Locate every Plasmodium ovale-infected red blood cell.
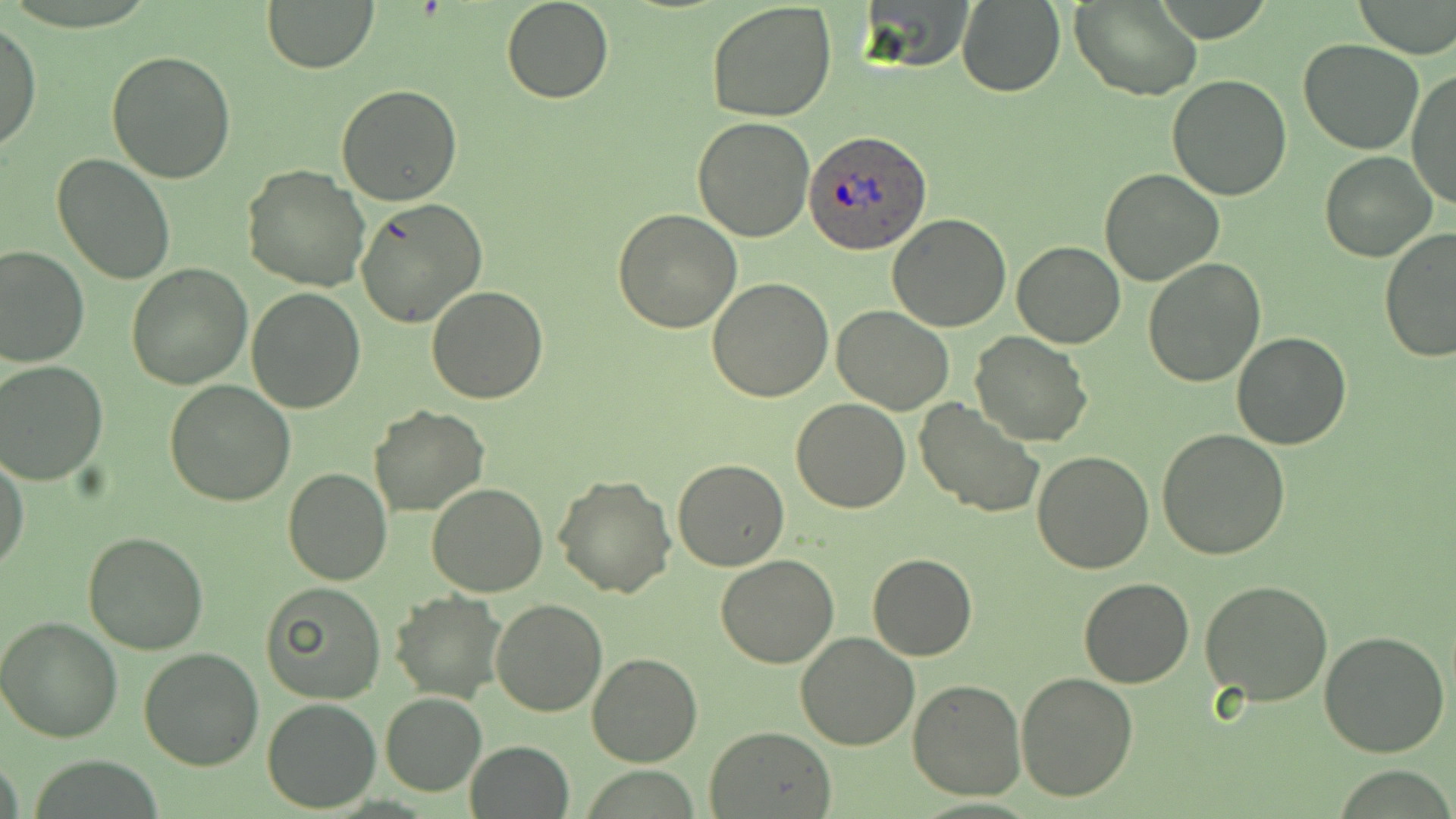

Approximate bounding boxes as [x1, y1, x2, y2] in pixels.
Plasmodium ovale-infected red blood cells: [804, 129, 932, 254].

{
  "slide_level_diagnosis": "Plasmodium ovale",
  "uninfected_red_blood_cell_locations": "approximate bounding boxes as [x1, y1, x2, y2] in pixels: [501, 0, 614, 104], [706, 0, 838, 120], [861, 0, 978, 72], [1352, 0, 1456, 58], [263, 1, 377, 73], [956, 1, 1067, 97], [1073, 2, 1202, 100], [1, 18, 40, 156], [1297, 39, 1424, 154], [106, 50, 237, 184], [1406, 68, 1456, 212], [1167, 76, 1293, 202], [335, 85, 463, 206], [692, 117, 816, 240], [1319, 150, 1437, 262], [52, 153, 178, 284], [243, 165, 370, 292], [1098, 167, 1225, 287], [355, 199, 488, 329], [613, 208, 743, 332], [887, 214, 1013, 332], [1378, 228, 1455, 363], [1012, 239, 1125, 348], [0, 245, 90, 367], [1143, 258, 1266, 388], [126, 264, 251, 389], [706, 279, 834, 403], [427, 285, 547, 403], [246, 287, 366, 413], [832, 306, 955, 415], [1232, 331, 1352, 451], [970, 332, 1091, 447], [1, 359, 110, 484], [166, 378, 295, 506], [792, 398, 910, 512], [914, 399, 1044, 519], [368, 404, 489, 516], [1158, 428, 1291, 559], [1, 450, 30, 576], [1030, 450, 1155, 574], [674, 459, 789, 571], [282, 467, 391, 586], [552, 472, 677, 597], [426, 483, 550, 597], [83, 530, 208, 655], [868, 553, 977, 660], [715, 556, 839, 669], [1199, 577, 1333, 706], [1079, 579, 1194, 688], [260, 581, 387, 703], [390, 591, 507, 702], [490, 599, 608, 717], [0, 614, 124, 741], [1318, 631, 1452, 757], [796, 632, 921, 750], [139, 647, 266, 770], [587, 651, 703, 768], [1015, 672, 1138, 802], [908, 679, 1025, 801], [380, 692, 486, 796], [262, 698, 380, 812], [704, 725, 837, 818], [467, 740, 573, 819]",
  "preparation": "thin blood film",
  "magnification": "1000x",
  "image_size": "1456×819 pixels",
  "modality": "optical microscopy",
  "field_of_view": "single",
  "stain": "May-Grünwald-Giemsa"
}